Name the parasite shown.
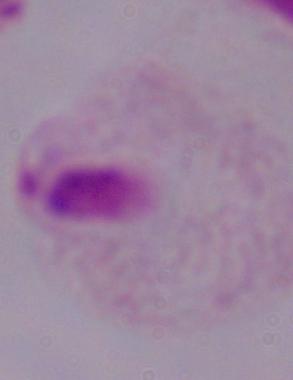
A trichomonad.

magnification = 1000x
modality = photomicrograph